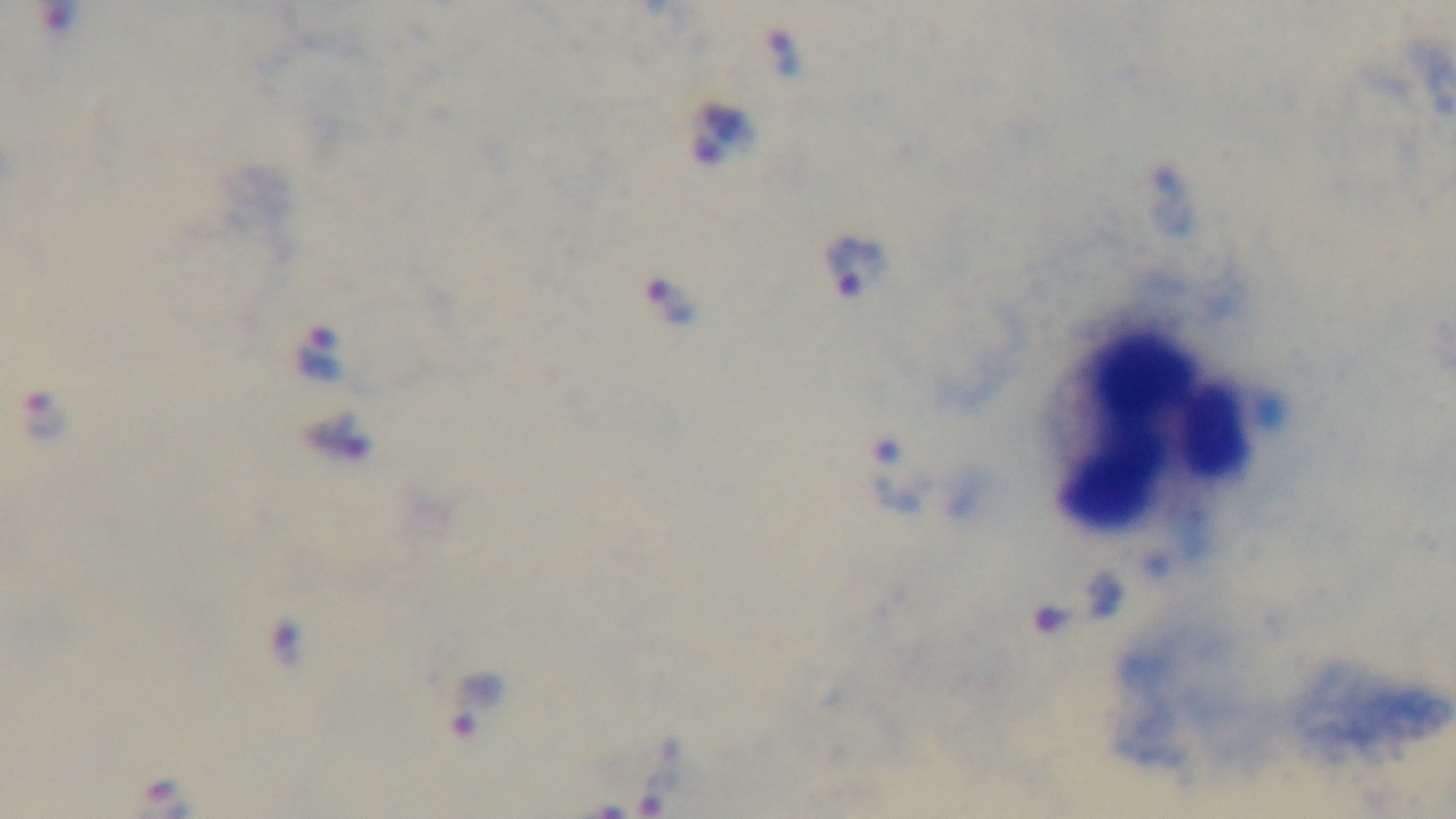

field of view = one from the slide
malaria status = infected
objective = 100x oil immersion
stain = Giemsa
modality = light microscopy
preparation = thick blood film
capture = mounted 4K digital camera